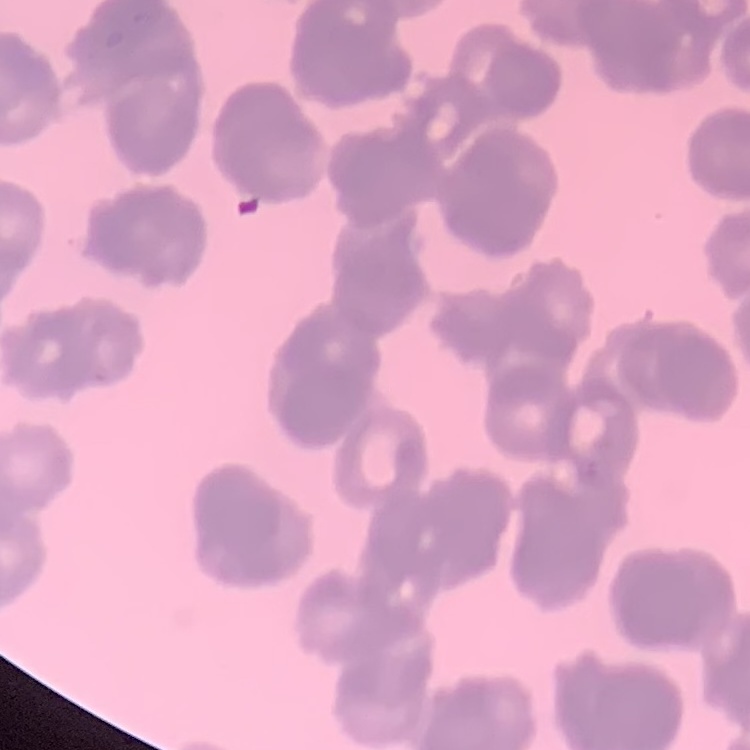
The erythrocytes show rouleaux formation. Stained with either Field's or Giemsa. One tile cut from a larger photomicrograph. Thin peripheral smear.